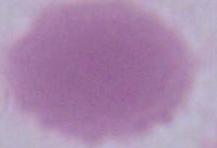
{
  "modality": "micrograph",
  "magnification": "1000x",
  "identification": "red blood cell"
}